Classify this cell by malaria status.
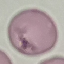

It is uninfected.

Summary:
  - Capture: smartphone camera at the microscope eyepiece
  - Image type: cell patch, automatically extracted from a larger field of view and resized to 64 × 64 pixels
  - Stain: Giemsa
  - Preparation: thin blood film